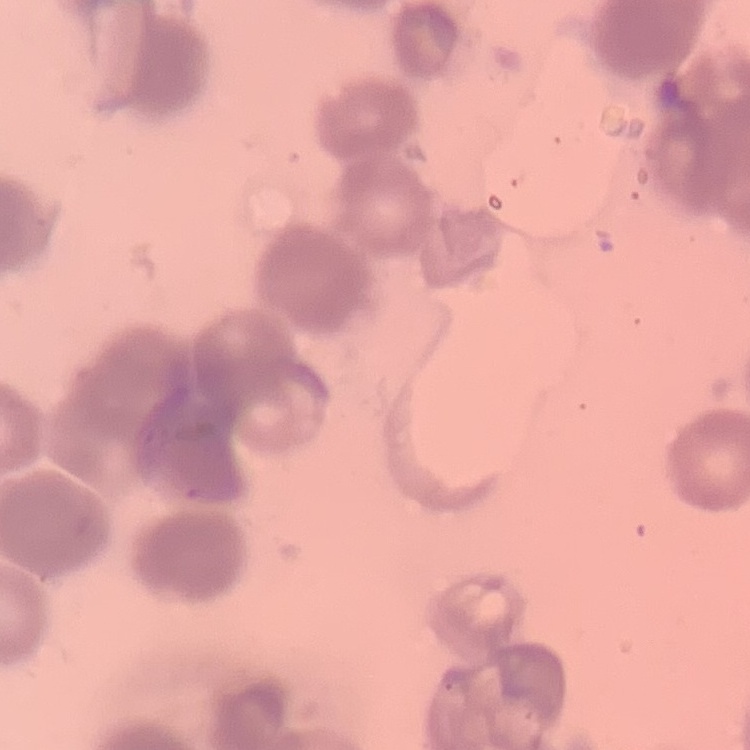 The red blood cells exhibit rouleaux formation. Thin blood smear. Square crop of a larger photomicrograph. Stained with either Field's or Giemsa.